Classify this cell by malaria status.
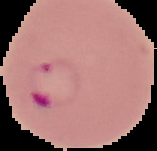

It is parasitized.

{
  "preparation": "thin blood smear",
  "image_type": "segmented cell region with the area outside set to black",
  "image_size": "157×151 pixels"
}